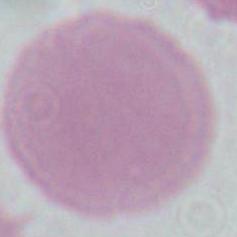
Summary:
  - Modality: micrograph
  - Magnification: 1000x
  - Identification: erythrocyte